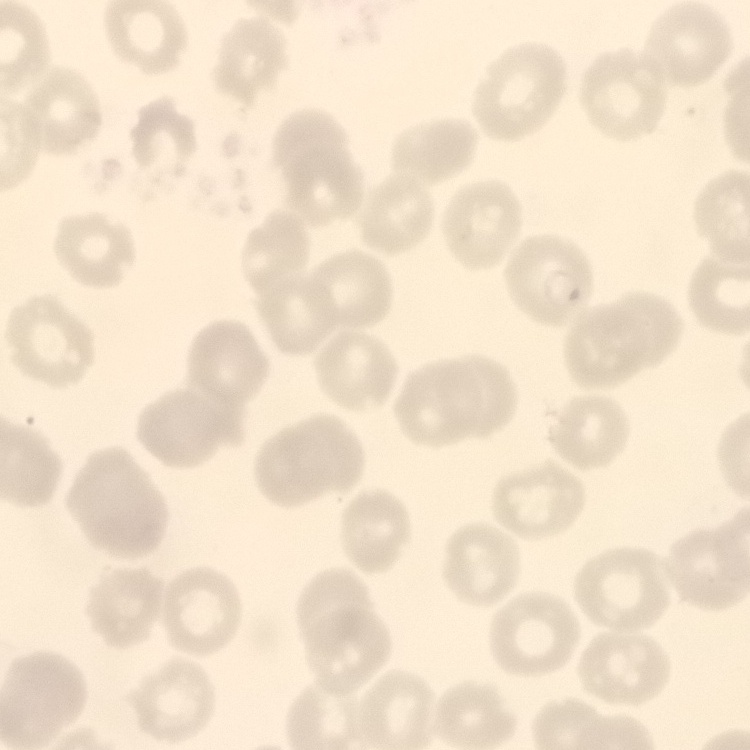
Summary:
  - Erythrocyte morphology: no rouleaux formation
  - Preparation: thin blood film
  - Image type: one tile cut from a larger photomicrograph
  - Stain: Field's or Giemsa